Locate every Plasmodium falciparum-infected red blood cell.
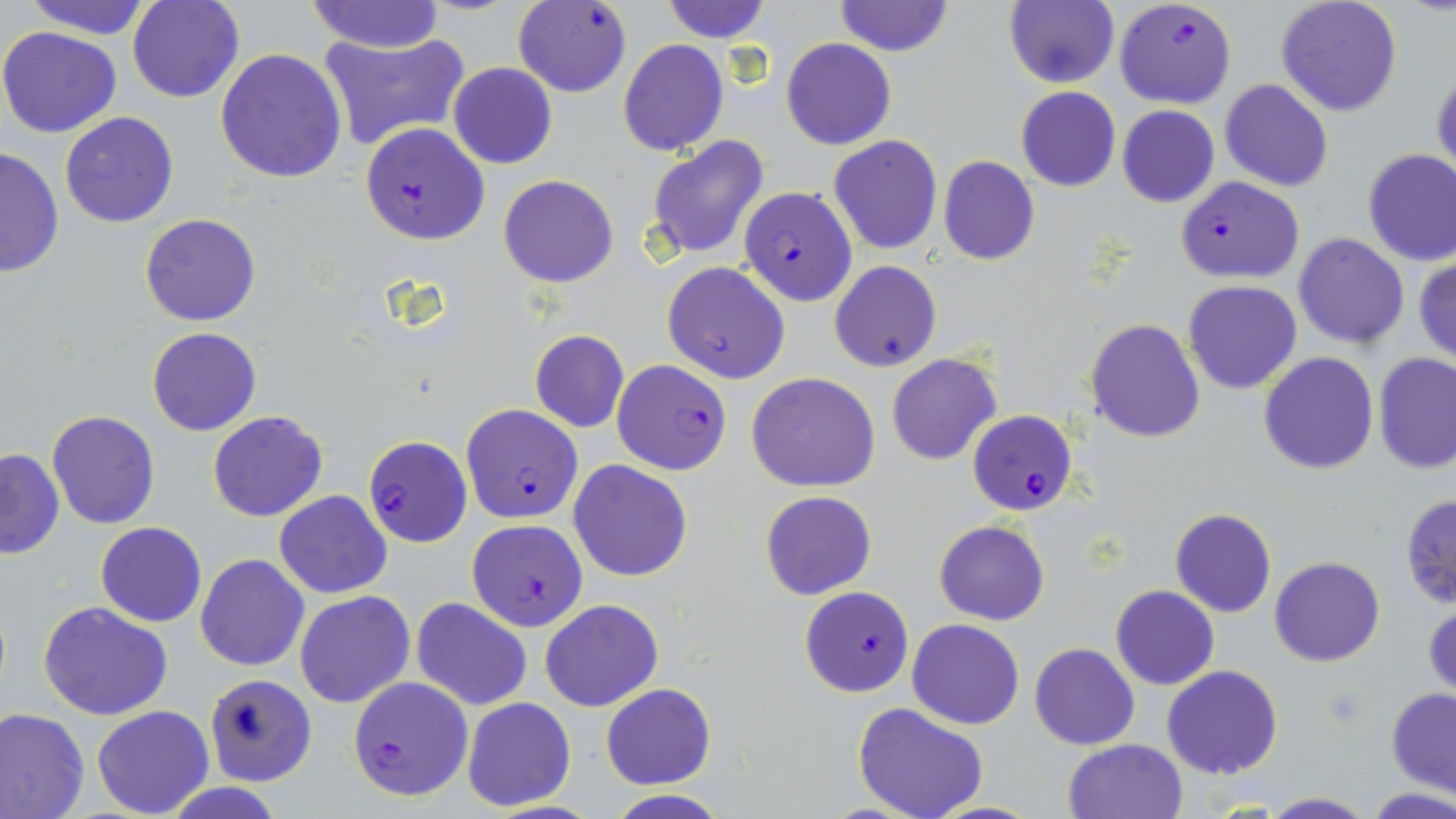

Approximate bounding boxes as (x1,y1)-(x2,y2) corner pairs in pixels.
Plasmodium falciparum-infected red blood cells: (514,0)-(632,97), (1114,0)-(1236,108), (358,123)-(490,244), (1177,176)-(1304,283), (726,190)-(854,325), (611,359)-(732,475), (460,404)-(582,523), (967,408)-(1079,517), (362,434)-(472,546), (467,519)-(587,631), (799,585)-(914,696), (347,675)-(473,801).

Uninfected red blood cell locations: (21,0)-(156,39), (129,0)-(244,103), (307,0)-(443,53), (659,0)-(772,44), (831,0)-(955,57), (1006,0)-(1120,89), (1275,0)-(1402,118), (0,26)-(123,138), (318,29)-(472,153), (618,38)-(730,158), (782,38)-(895,151), (215,48)-(347,183), (448,63)-(557,169), (1432,63)-(1455,180), (1220,79)-(1334,193), (1015,86)-(1122,192), (1117,106)-(1218,208), (59,111)-(179,227), (645,134)-(771,262), (829,134)-(943,255), (1,145)-(63,281), (1362,148)-(1456,267), (938,155)-(1039,265), (498,173)-(619,287), (1320,194)-(1444,338), (140,212)-(262,326), (1293,232)-(1409,349), (1414,256)-(1456,364), (829,260)-(942,372), (662,261)-(791,384), (1182,279)-(1302,394), (1085,318)-(1206,442), (147,327)-(261,436), (529,330)-(629,433), (891,348)-(1007,459), (1259,353)-(1379,475), (1374,353)-(1455,476), (747,372)-(880,493), (46,410)-(161,530), (207,410)-(328,522), (1,448)-(64,559), (568,459)-(692,583), (275,490)-(392,598), (759,490)-(877,601), (1400,492)-(1455,609), (1168,507)-(1277,617), (934,520)-(1049,625), (96,521)-(205,626), (196,553)-(309,671), (1270,556)-(1385,667), (1110,585)-(1219,690), (296,590)-(415,708), (412,597)-(531,711), (38,599)-(173,721), (540,599)-(663,712), (1424,599)-(1455,701), (907,619)-(1025,730), (1029,643)-(1140,750), (1161,664)-(1283,780), (202,672)-(318,787), (601,683)-(715,789), (1386,688)-(1456,796), (460,697)-(577,811), (853,702)-(989,819), (92,705)-(214,816), (0,707)-(90,819), (1062,738)-(1188,819), (602,791)-(731,819), (1257,792)-(1377,818). Slide-level diagnosis: Plasmodium falciparum. Light microscopy. Image is 1456×819 pixels. Thin blood film. 1000x magnification. Single field of view. May-Grünwald-Giemsa-stained preparation.